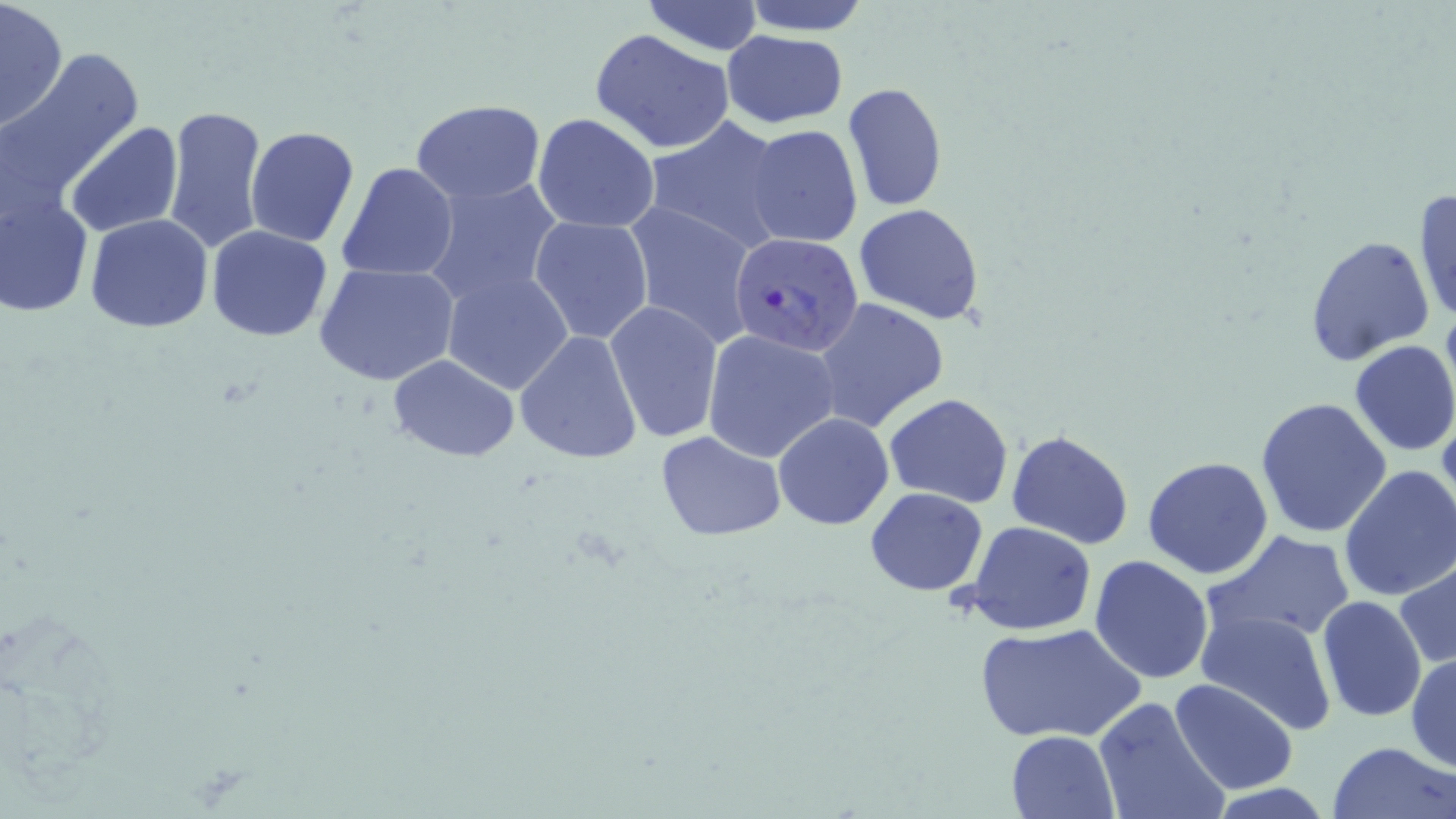
Approximate bounding boxes as (x1,y1)-(x2,y2) corner pairs in pixels. Uninfected red blood cell locations: (0,0)-(69,131), (640,0)-(766,55), (740,0)-(873,35), (588,28)-(737,153), (720,30)-(848,128), (6,49)-(144,196), (842,81)-(949,212), (412,100)-(545,204), (162,105)-(269,254), (532,113)-(660,234), (643,116)-(791,251), (65,122)-(182,238), (745,124)-(863,248), (243,126)-(359,246), (338,161)-(459,282), (0,172)-(96,322), (419,177)-(563,307), (1412,186)-(1455,326), (623,200)-(758,347), (853,203)-(986,323), (85,214)-(214,333), (529,216)-(654,344), (206,225)-(335,343), (1305,234)-(1435,365), (316,263)-(459,387), (440,268)-(575,396), (813,297)-(949,433), (605,301)-(723,443), (702,329)-(841,462), (515,330)-(642,465), (1348,339)-(1456,457), (387,354)-(519,461), (883,393)-(1014,509), (1256,398)-(1393,540), (773,412)-(894,530), (1005,429)-(1133,550), (654,430)-(786,541), (1142,455)-(1275,578), (1338,464)-(1456,603), (865,487)-(989,596), (967,522)-(1098,635), (1202,530)-(1357,646), (1089,554)-(1216,685), (1394,556)-(1456,670), (1231,558)-(1384,703), (1317,596)-(1427,722), (1197,609)-(1337,733), (973,621)-(1146,744), (1408,653)-(1455,772), (1169,678)-(1297,797), (1092,695)-(1231,819), (1006,730)-(1122,818), (1327,740)-(1456,819). Plasmodium falciparum-infected red blood cell locations: (729,231)-(864,360). Slide-level diagnosis: Plasmodium falciparum. May-Grünwald-Giemsa stain. Image is 1456×819 pixels. Light microscopy. One field of a larger specimen. Thin blood film. 1000x magnification.